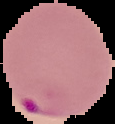

image_size: 115×124 pixels
image_type: segmented cell region with the area outside set to black
malaria_status: parasitized
preparation: thin blood smear